Name the parasite shown.
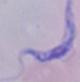

A trypanosome.

Summary:
  - Modality: photomicrograph
  - Magnification: 1000x